Outline each blood parasite and name the species.
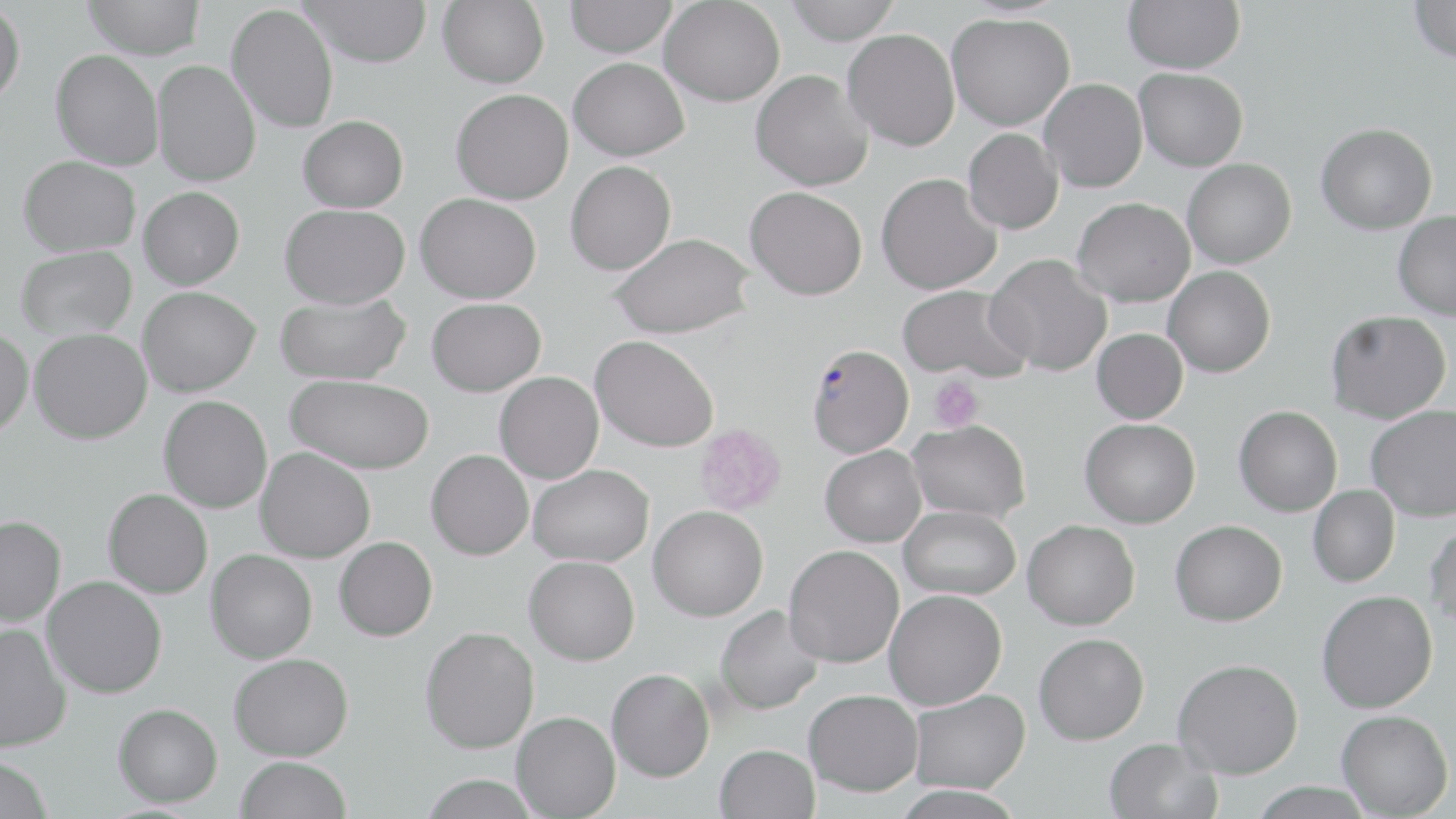

Approximate bounding boxes as [x1, y1, x2, y2] in pixels.
Plasmodium falciparum-infected red blood cells: [806, 343, 914, 458].
No Plasmodium ovale, Plasmodium malariae, Plasmodium vivax, Babesia divergens, or Trypanosoma brucei observed.

{
  "slide_level_diagnosis": "Plasmodium falciparum",
  "stain": "May-Grünwald-Giemsa",
  "modality": "optical microscopy",
  "preparation": "thin blood smear",
  "magnification": "1000x",
  "uninfected_red_blood_cell_locations": "approximate bounding boxes as [x1, y1, x2, y2] in pixels: [82, 0, 205, 59], [300, 0, 433, 67], [437, 0, 549, 88], [564, 0, 677, 57], [782, 0, 900, 44], [1123, 0, 1245, 74], [1408, 0, 1456, 63], [0, 1, 25, 107], [660, 1, 785, 106], [227, 4, 339, 133], [947, 13, 1075, 130], [843, 28, 960, 151], [51, 49, 164, 170], [569, 57, 689, 161], [152, 60, 261, 186], [1135, 68, 1248, 172], [750, 69, 874, 190], [1039, 78, 1148, 193], [451, 88, 573, 204], [298, 115, 408, 212], [1316, 122, 1438, 235], [962, 128, 1063, 234], [19, 155, 141, 256], [1182, 158, 1297, 268], [565, 160, 676, 275], [876, 173, 1001, 294], [745, 185, 868, 300], [138, 186, 244, 289], [416, 193, 541, 303], [1072, 196, 1195, 306], [280, 203, 410, 309], [1393, 211, 1456, 320], [608, 232, 754, 339], [16, 246, 137, 340], [986, 253, 1112, 376], [1163, 266, 1275, 378], [897, 284, 1033, 382], [138, 286, 260, 396], [275, 291, 411, 385], [427, 298, 545, 396], [1326, 310, 1451, 424], [0, 327, 33, 438], [29, 328, 152, 444], [1092, 328, 1187, 424], [590, 335, 719, 452], [495, 371, 604, 483], [286, 375, 434, 474], [159, 395, 272, 513], [1366, 404, 1456, 521], [1234, 405, 1342, 516], [1080, 418, 1200, 528], [907, 419, 1031, 522], [820, 444, 926, 547], [255, 447, 375, 563], [426, 449, 533, 560], [529, 463, 653, 566], [1308, 485, 1400, 587], [103, 488, 213, 598], [648, 505, 768, 621], [899, 505, 1020, 600], [0, 515, 66, 626], [1425, 518, 1456, 629], [1022, 519, 1140, 630], [1170, 520, 1287, 626], [334, 537, 437, 641], [784, 544, 904, 668], [205, 549, 317, 663], [524, 555, 640, 665], [42, 575, 167, 698], [884, 589, 1007, 710], [1317, 589, 1438, 713], [714, 605, 824, 715], [0, 623, 71, 752], [420, 626, 539, 753], [1034, 632, 1149, 744], [229, 653, 353, 761], [1172, 658, 1304, 778], [606, 668, 714, 781], [804, 689, 923, 796], [909, 689, 1031, 793], [113, 703, 223, 807], [1336, 709, 1453, 817], [511, 711, 620, 818], [1103, 738, 1222, 819], [714, 744, 819, 819], [0, 755, 55, 819], [236, 756, 352, 819], [418, 774, 543, 819], [1248, 781, 1376, 819]",
  "platelet_locations": "approximate bounding boxes as [x1, y1, x2, y2] in pixels: [928, 375, 984, 432], [694, 423, 786, 515]",
  "field_of_view": "single",
  "image_size": "1456×819 pixels"
}